Assess this cell for malaria.
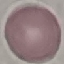

Uninfected.

Summary:
  - Stain: Giemsa
  - Preparation: thin smear
  - Image type: automatically extracted cell patch, resized to 64 × 64 pixels
  - Capture: smartphone camera at the microscope eyepiece